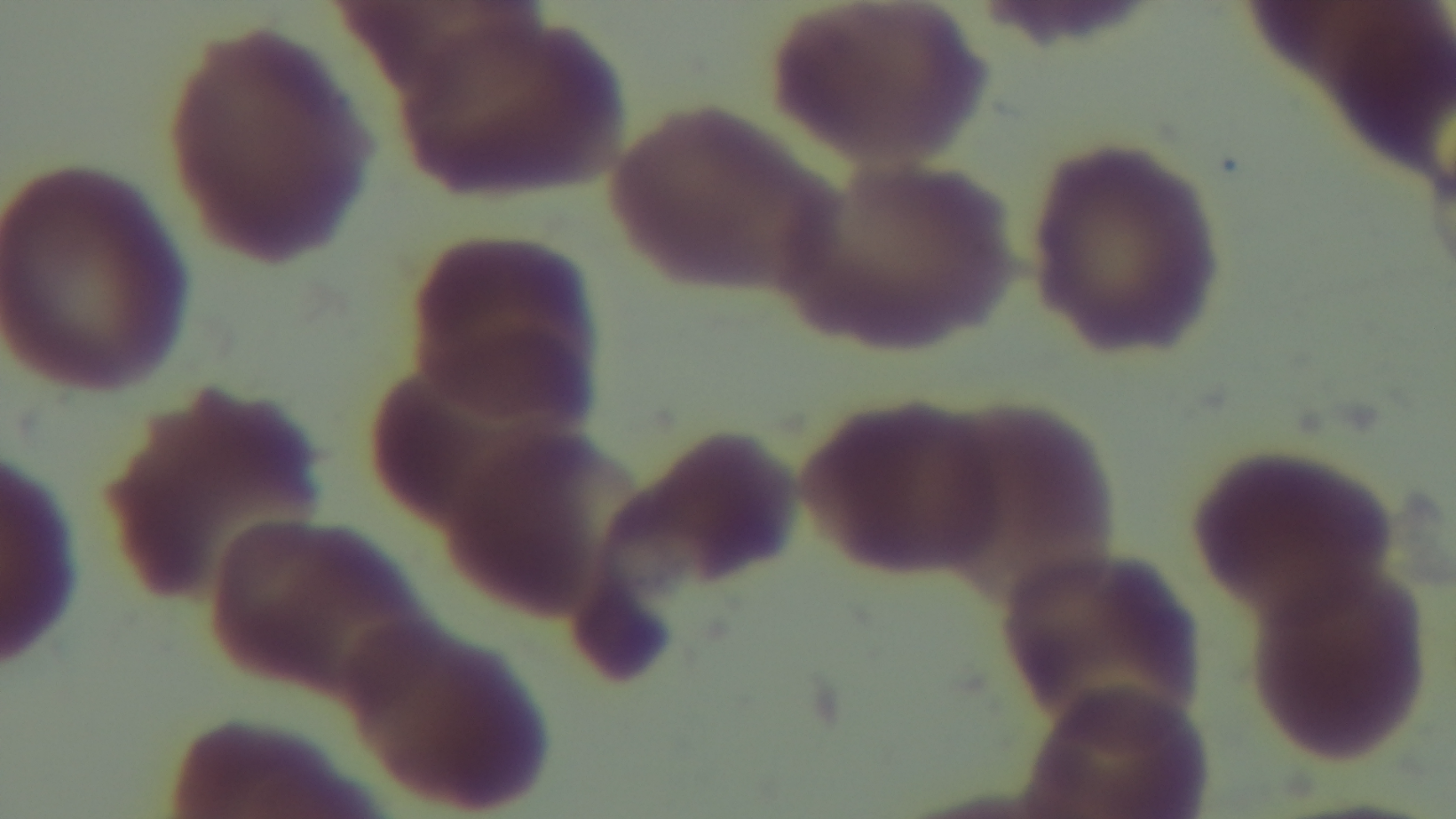
{
  "malaria_status": "uninfected",
  "capture": "mounted 4K digital camera",
  "field_of_view": "one from the slide",
  "stain": "Giemsa",
  "preparation": "thin",
  "modality": "light microscopy",
  "objective": "100x oil immersion"
}